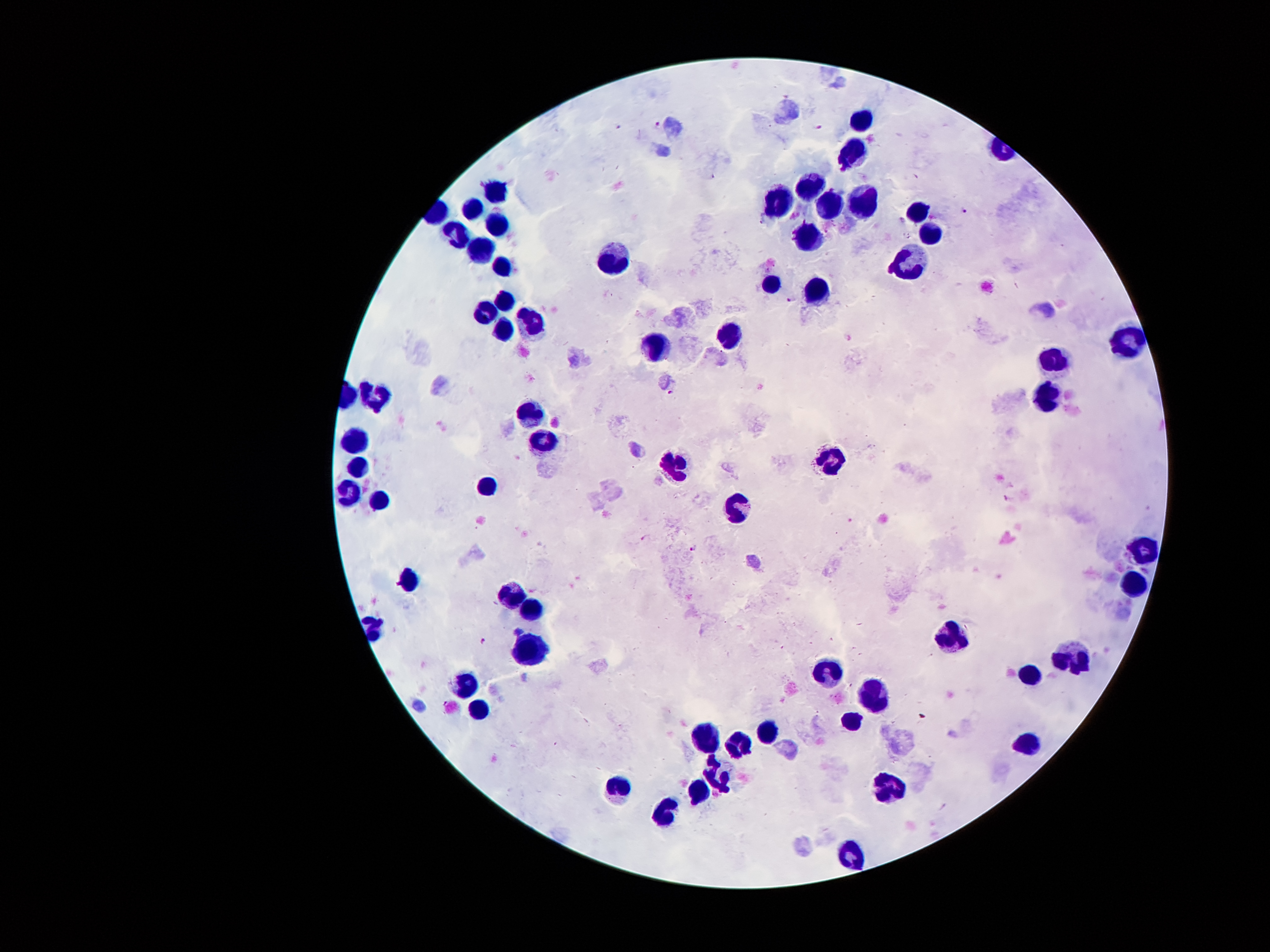
Approximate centers as [x, y] in pixels.
Summary:
  - Malaria parasite locations: [657, 125], [619, 126], [817, 128], [965, 212], [903, 220], [791, 299], [672, 392], [1007, 499], [646, 538], [691, 548], [483, 641]
  - Leukocyte locations: [861, 119], [851, 153], [808, 183], [496, 190], [777, 196], [859, 200], [828, 202], [920, 204], [467, 205], [498, 229], [929, 235], [804, 236], [453, 237], [483, 250], [615, 258], [500, 263], [909, 264], [771, 285], [817, 287], [504, 300], [485, 309], [533, 320], [505, 329], [729, 332], [1130, 339], [655, 346], [1053, 360], [1044, 399], [369, 400], [526, 412], [541, 437], [354, 445], [830, 459], [360, 468], [677, 468], [488, 488], [347, 489], [377, 495], [1139, 547], [401, 580], [514, 597], [528, 610], [950, 640], [530, 652], [1068, 658], [829, 667], [1025, 673], [469, 683], [878, 695], [484, 711], [853, 718], [765, 727], [706, 735], [1028, 742], [740, 745], [717, 778], [886, 787], [700, 788], [621, 796], [670, 807], [849, 850]
  - Image size: 1270×952 pixels
  - Field of view: one from this slide
  - Preparation: thick blood smear
  - Stain: Giemsa
  - Capture: smartphone through the microscope eyepiece
  - Patient malaria status: infected with Plasmodium falciparum
  - Magnification: 100x